Locate platelets.
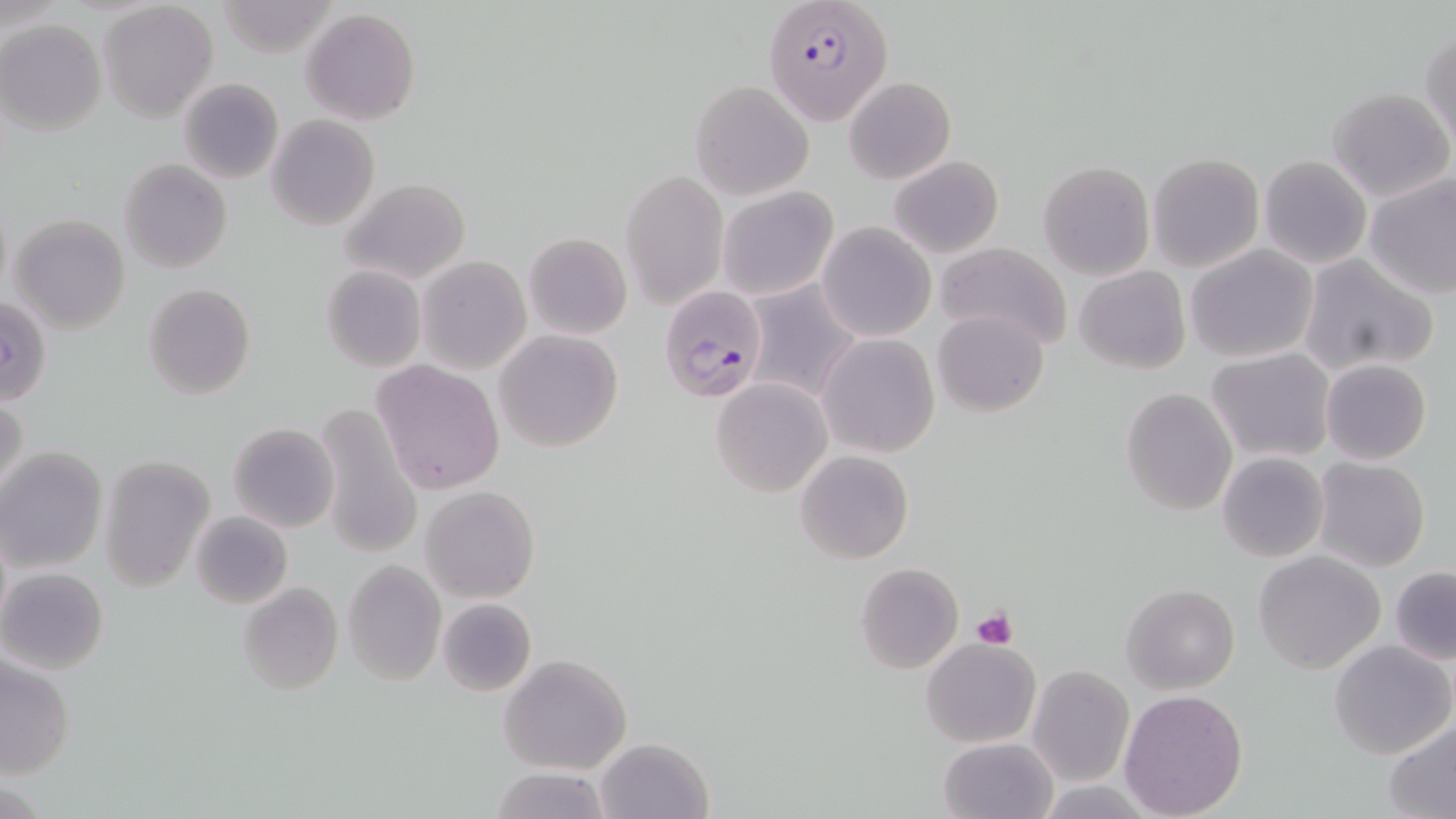

Approximate bounding boxes as [x1, y1, x2, y2] in pixels.
Platelets: [972, 606, 1018, 649].

slide-level diagnosis = Plasmodium falciparum
magnification = 1000x
modality = light microscopy
Plasmodium falciparum-infected red blood cell locations = approximate bounding boxes as [x1, y1, x2, y2] in pixels: [764, 0, 894, 129], [659, 286, 770, 404]
image size = 1456×819 pixels
uninfected red blood cell locations = approximate bounding boxes as [x1, y1, x2, y2] in pixels: [99, 3, 218, 121], [300, 9, 421, 124], [1, 20, 105, 135], [1422, 28, 1455, 149], [844, 76, 955, 183], [179, 77, 284, 184], [690, 79, 815, 199], [1327, 87, 1454, 202], [265, 115, 379, 231], [1148, 153, 1263, 271], [888, 155, 1005, 258], [1259, 156, 1372, 269], [118, 158, 232, 273], [1037, 161, 1156, 281], [621, 169, 728, 309], [1365, 175, 1456, 300], [341, 177, 471, 284], [717, 185, 837, 301], [9, 214, 131, 333], [817, 222, 936, 342], [524, 232, 632, 339], [934, 241, 1074, 350], [1185, 244, 1319, 363], [1299, 254, 1436, 376], [417, 256, 531, 374], [321, 264, 426, 372], [1075, 265, 1191, 375], [143, 283, 255, 400], [742, 283, 862, 403], [933, 309, 1049, 416], [494, 329, 624, 454], [818, 333, 940, 457], [1205, 347, 1336, 463], [1321, 359, 1433, 465], [371, 360, 505, 495], [711, 378, 832, 497], [1120, 387, 1237, 516], [1, 392, 28, 504], [313, 400, 423, 559], [228, 423, 339, 532], [1, 447, 109, 573], [795, 450, 913, 564], [1217, 452, 1328, 562], [99, 456, 214, 592], [1313, 456, 1430, 571], [422, 485, 540, 602], [190, 510, 293, 609], [1252, 551, 1387, 675], [341, 561, 446, 684], [855, 563, 963, 674], [1389, 566, 1456, 665], [0, 567, 109, 675], [238, 581, 342, 696], [1122, 582, 1239, 694], [438, 598, 537, 696], [449, 609, 582, 728], [922, 637, 1040, 748], [1328, 639, 1456, 759], [499, 653, 634, 775], [1, 656, 75, 779], [1027, 664, 1134, 786], [1119, 689, 1249, 818], [1383, 719, 1456, 817], [595, 736, 714, 819], [938, 737, 1057, 818], [489, 766, 613, 819]
stain = May-Grünwald-Giemsa
preparation = thin blood smear
field of view = single